Evaluate for parasitized red blood cells.
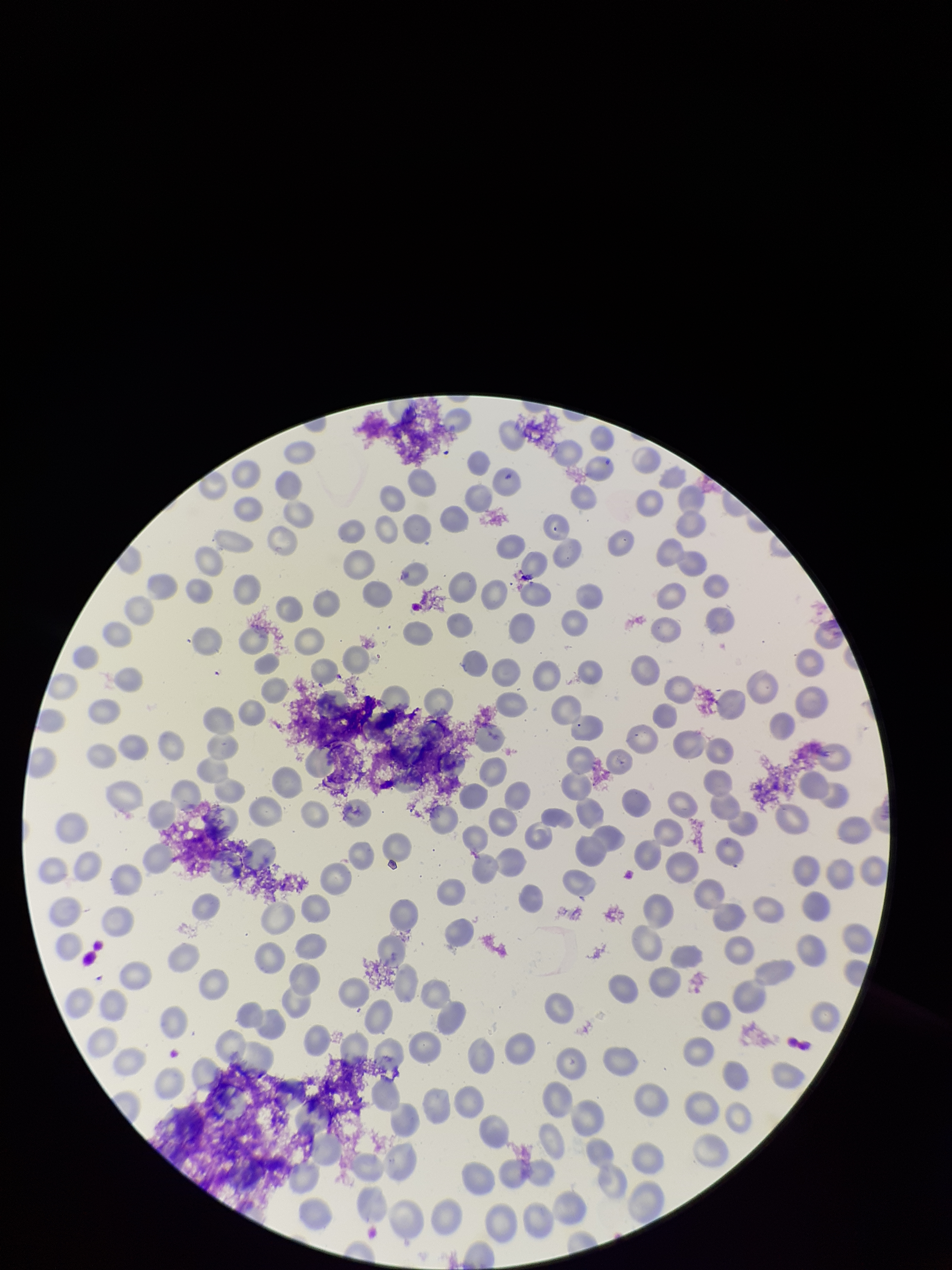
None identified.

Image is 952×1270 pixels. Stained with Giemsa. Parasitized red blood cell count: 0. Preparation: thin smear. One field from this slide. Red blood cell count: 196. Photographed through the microscope eyepiece with a smartphone camera. Patient malaria status: negative.